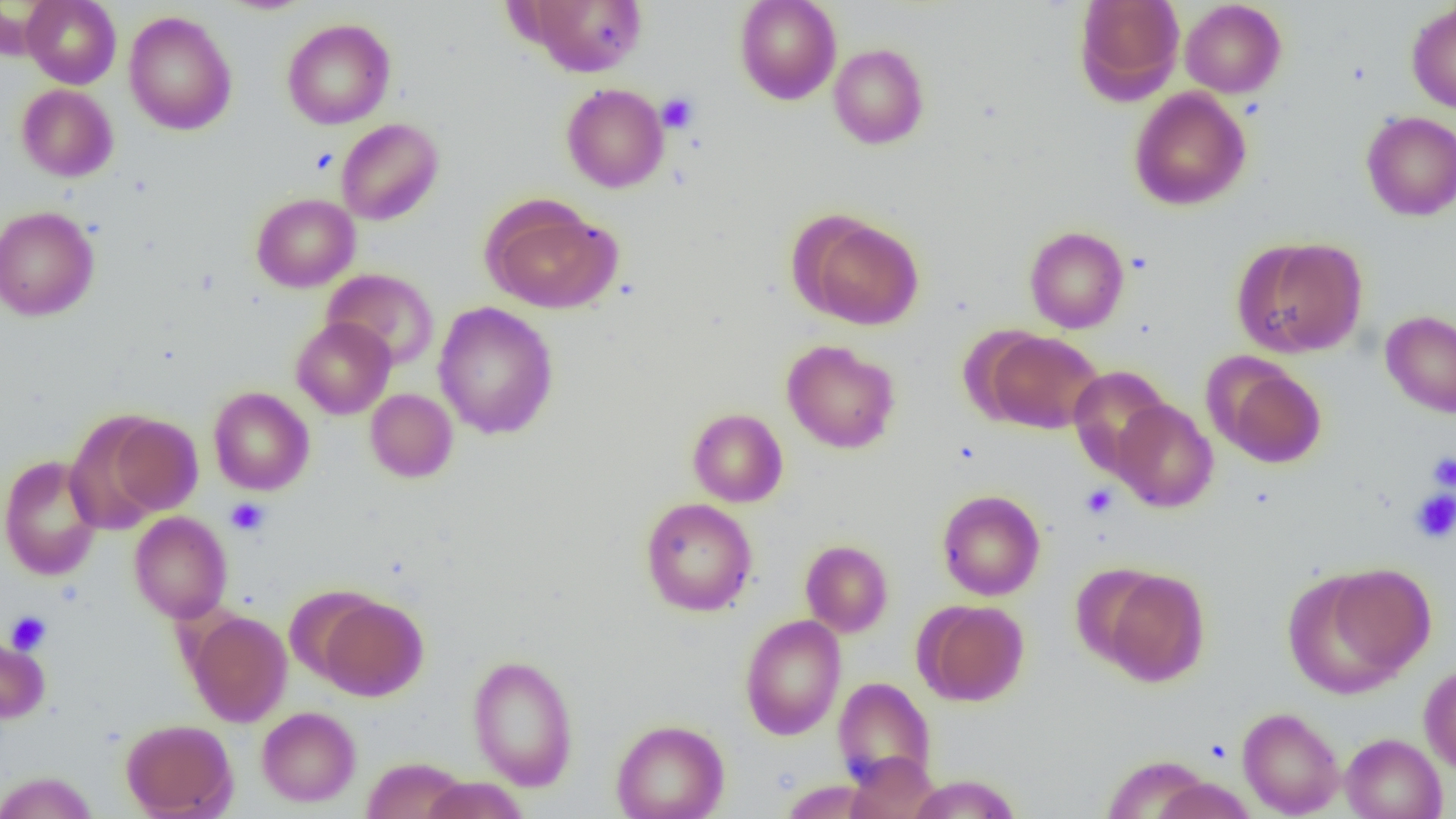

Summary:
  - Coordinate format: approximate bounding boxes as (x1, y1, x2, y2) in pixels
  - Uninfected red blood cell locations: (22, 0, 121, 89), (218, 0, 315, 14), (522, 0, 648, 76), (734, 0, 842, 104), (1074, 0, 1186, 103), (1180, 1, 1286, 98), (1406, 2, 1456, 114), (123, 11, 237, 135), (282, 18, 395, 129), (828, 43, 930, 149), (561, 83, 669, 193), (17, 84, 118, 182), (1130, 87, 1252, 211), (1361, 111, 1456, 221), (336, 119, 443, 225), (251, 193, 360, 292), (484, 199, 620, 313), (0, 206, 100, 321), (800, 215, 925, 330), (1024, 226, 1129, 333), (1235, 237, 1368, 357), (322, 268, 439, 370), (433, 302, 558, 439), (1380, 310, 1456, 418), (291, 317, 395, 419), (983, 329, 1103, 434), (781, 339, 900, 454), (1215, 361, 1327, 468), (1068, 365, 1172, 475), (208, 387, 314, 495), (365, 388, 458, 482), (1112, 399, 1218, 512), (687, 408, 788, 507), (98, 413, 203, 518), (0, 454, 104, 581), (936, 490, 1045, 601), (640, 497, 757, 616), (129, 511, 232, 623), (800, 539, 893, 637), (1292, 565, 1433, 692), (1097, 566, 1211, 687), (317, 595, 428, 701), (916, 600, 1029, 706), (185, 610, 292, 727), (740, 613, 847, 740), (0, 634, 49, 723), (466, 654, 579, 791), (1419, 664, 1456, 774), (833, 676, 936, 788), (257, 706, 360, 807), (1237, 707, 1345, 818), (121, 719, 236, 818), (611, 719, 729, 819), (1340, 733, 1448, 819), (845, 752, 940, 817), (1102, 754, 1215, 817), (362, 756, 469, 819), (0, 771, 98, 819), (907, 774, 1021, 818), (421, 777, 529, 818), (1149, 777, 1259, 819), (779, 780, 880, 818)
  - Platelet locations: (657, 92, 699, 133), (1427, 452, 1456, 491), (1081, 484, 1117, 518), (1410, 489, 1456, 543), (225, 497, 270, 536), (5, 611, 52, 654)
  - Slide-level diagnosis: no evidence of blood parasites
  - Magnification: 1000x
  - Field of view: one of a larger specimen
  - Preparation: thin blood film
  - Image size: 1456×819 pixels
  - Modality: optical microscopy